Identify the parasite.
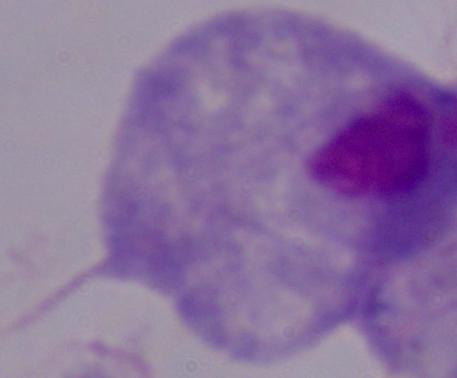

A trichomonad.

Summary:
  - Modality: micrograph
  - Magnification: 1000x